Locate every Plasmodium parasite.
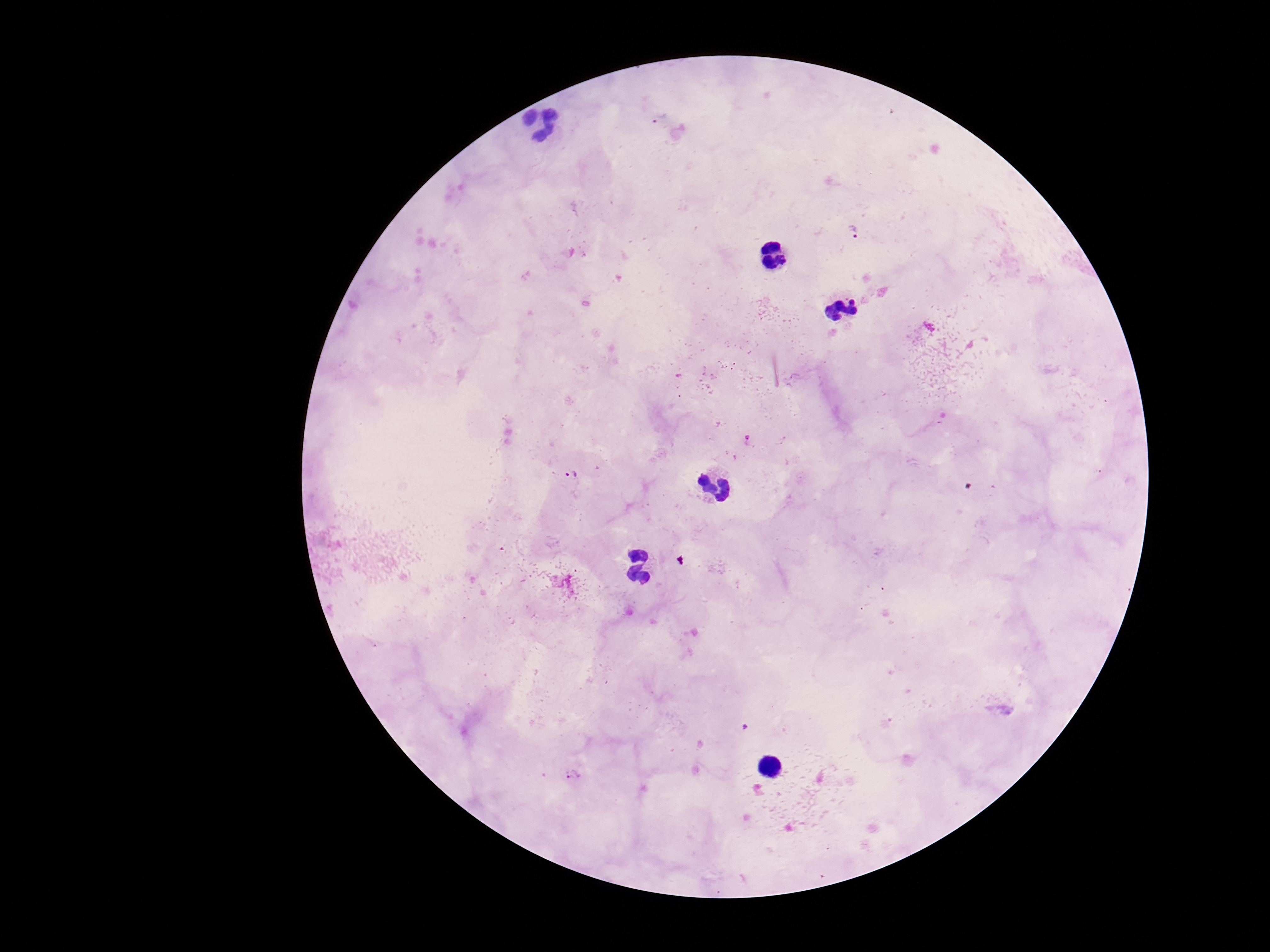
Approximate object centers, in pixels from the top-left corner.
Plasmodium parasites: (x=855, y=230), (x=748, y=437), (x=571, y=474), (x=573, y=775).

Thick peripheral-blood smear. Single field of view. Patient malaria status: infected. Giemsa-stained preparation. Image is 1270×952 pixels. Photographed through the microscope eyepiece with a smartphone camera. 100x magnification.